Describe the morphology of the red blood cells.
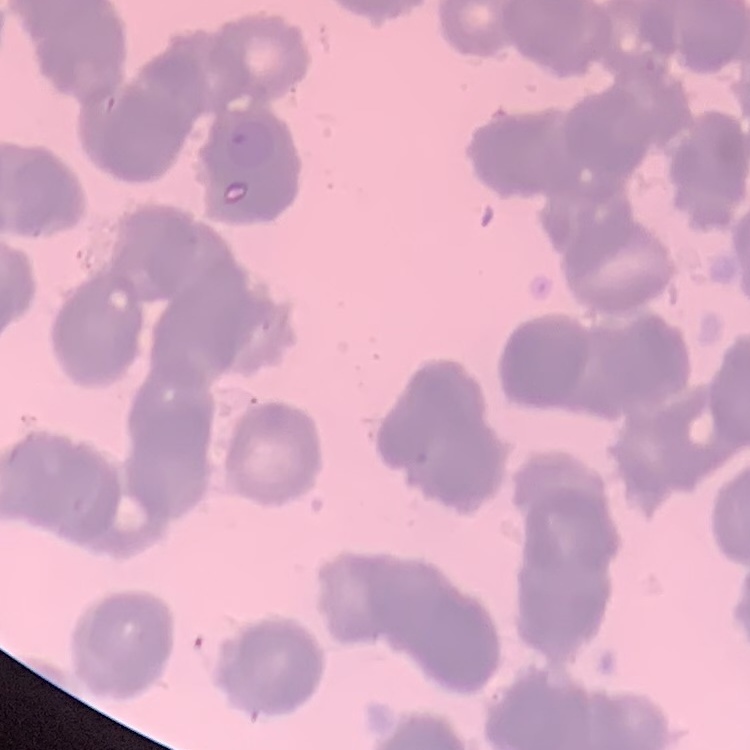
They show rouleaux formation.

Thin peripheral smear. Stained with either Field's or Giemsa. Square crop of a larger photomicrograph.